Outline each blood parasite and name the species.
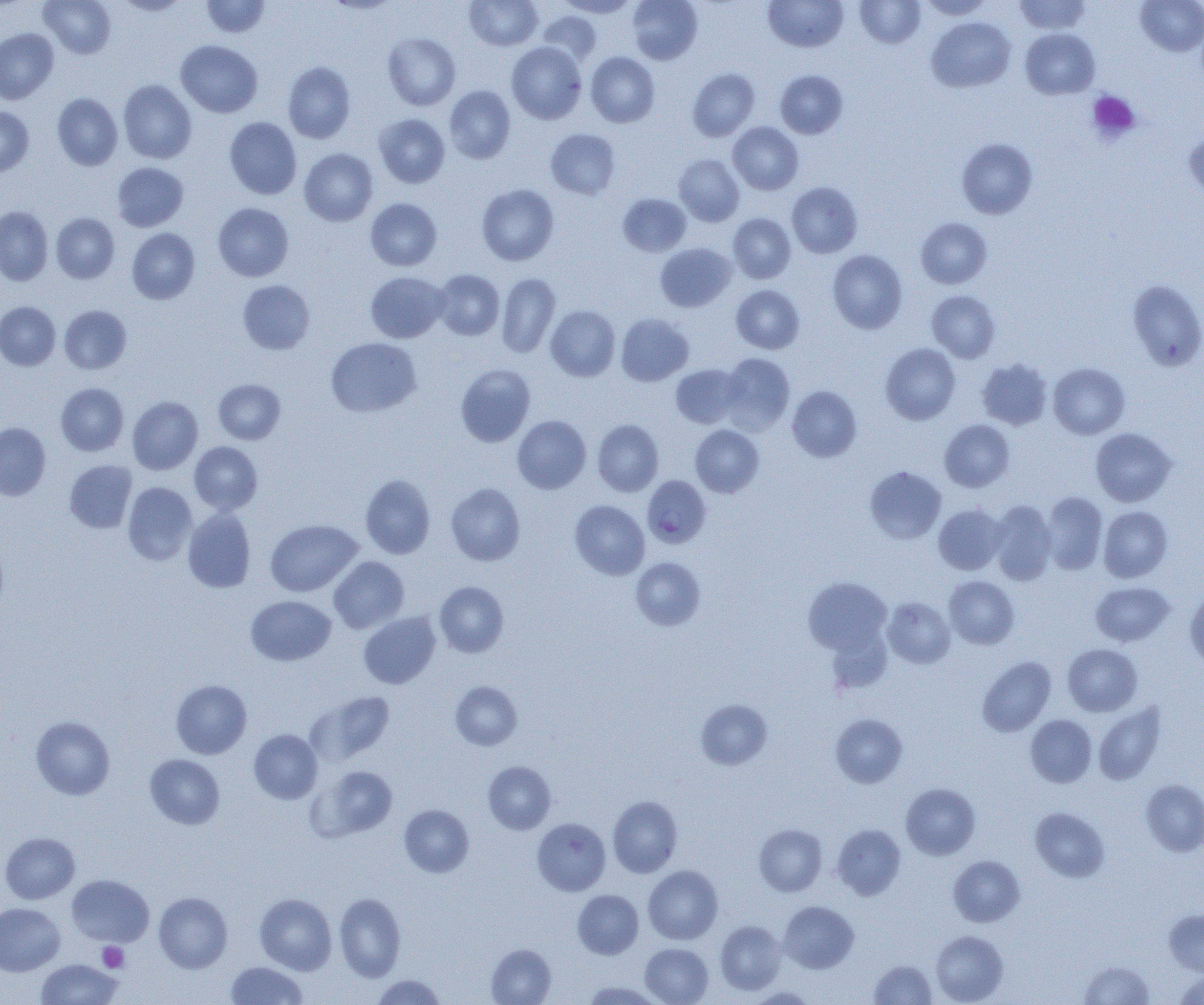

Approximate bounding boxes as (x1,y1)-(x2,y2) corner pairs in pixels.
Plasmodium falciparum-infected red blood cells: (642,475)-(711,548).
No Plasmodium ovale, Plasmodium malariae, Plasmodium vivax, Babesia divergens, or Trypanosoma brucei observed.

Summary:
  - Uninfected red blood cell locations: (39,0)-(116,59), (112,0)-(190,15), (201,0)-(270,38), (324,0)-(401,15), (464,0)-(543,51), (556,0)-(638,18), (626,0)-(703,65), (855,0)-(925,48), (920,0)-(995,19), (1014,0)-(1091,34), (1136,0)-(1204,56), (763,1)-(848,52), (537,12)-(602,66), (926,17)-(1015,92), (0,28)-(59,104), (1020,28)-(1100,99), (383,32)-(460,111), (175,40)-(262,118), (506,42)-(586,124), (586,52)-(660,128), (283,61)-(356,144), (687,67)-(760,141), (775,70)-(848,138), (118,79)-(197,164), (444,85)-(516,164), (52,93)-(123,170), (0,106)-(33,176), (374,114)-(450,188), (224,117)-(302,199), (728,122)-(803,195), (545,128)-(621,200), (1183,131)-(1204,205), (957,138)-(1038,219), (299,148)-(378,226), (673,154)-(744,226), (112,162)-(188,232), (786,182)-(863,257), (476,183)-(559,266), (618,194)-(691,256), (365,198)-(442,271), (213,202)-(294,281), (0,206)-(53,285), (51,212)-(119,284), (728,213)-(795,283), (915,217)-(992,289), (127,228)-(200,304), (655,242)-(736,312), (827,250)-(907,334), (432,269)-(504,340), (365,271)-(448,343), (496,273)-(560,358), (238,280)-(315,354), (1127,280)-(1204,370), (731,285)-(804,353), (927,290)-(1000,363), (0,301)-(60,370), (59,305)-(131,374), (546,305)-(620,381), (616,313)-(694,385), (325,337)-(421,417), (881,343)-(960,425), (719,353)-(795,434), (977,357)-(1053,430), (1048,363)-(1130,439), (455,364)-(536,447), (671,364)-(744,429), (213,379)-(286,444), (55,383)-(128,456), (787,386)-(861,462), (127,396)-(202,475), (512,415)-(591,494), (592,420)-(664,496), (939,420)-(1014,492), (0,422)-(51,501), (690,425)-(764,497), (1090,428)-(1177,507), (189,441)-(263,514), (64,460)-(136,534), (864,466)-(946,544), (360,474)-(435,559), (122,482)-(197,565), (446,483)-(525,566), (1040,491)-(1108,575), (569,500)-(650,579), (988,501)-(1057,585), (933,504)-(1007,575), (1098,505)-(1172,582), (182,508)-(255,592), (265,519)-(362,597), (0,543)-(9,616), (328,556)-(409,634), (631,557)-(706,631), (943,576)-(1019,649), (803,577)-(892,656), (434,581)-(508,657), (1089,581)-(1174,647), (1184,589)-(1204,669), (246,595)-(336,666), (882,597)-(955,668), (358,612)-(441,689), (1062,643)-(1142,716), (977,656)-(1056,736), (171,680)-(251,759), (450,681)-(522,750), (307,691)-(395,765), (695,699)-(772,769), (1093,703)-(1166,785), (830,713)-(907,788), (1025,714)-(1097,788), (31,716)-(115,799), (249,729)-(322,804), (145,754)-(225,829), (483,760)-(556,834), (311,765)-(398,840), (1141,779)-(1204,856), (900,783)-(980,859), (607,795)-(682,877), (399,804)-(473,877), (1030,807)-(1110,882), (532,817)-(611,896), (754,824)-(827,896), (832,824)-(906,900), (0,832)-(80,904), (948,855)-(1024,927), (643,865)-(723,944), (67,874)-(154,947), (572,890)-(643,959), (153,892)-(232,973), (255,893)-(336,975), (334,893)-(406,981), (779,901)-(859,973), (0,902)-(65,975), (1164,909)-(1204,976), (715,920)-(786,995), (931,930)-(1008,1004), (486,943)-(556,1005), (640,943)-(713,1005), (36,958)-(123,1005), (870,960)-(937,1004), (1079,960)-(1154,1004), (226,961)-(307,1005), (1173,971)-(1204,1005), (371,975)-(446,1004), (582,981)-(663,1005), (747,987)-(817,1004)
  - Platelet locations: (1087,91)-(1141,144), (97,942)-(129,972)
  - Slide-level diagnosis: Plasmodium falciparum
  - Modality: optical microscopy
  - Field of view: single
  - Preparation: thin blood film
  - Magnification: 1000x
  - Image size: 1204×1005 pixels